Outline each Plasmodium falciparum-infected red blood cell.
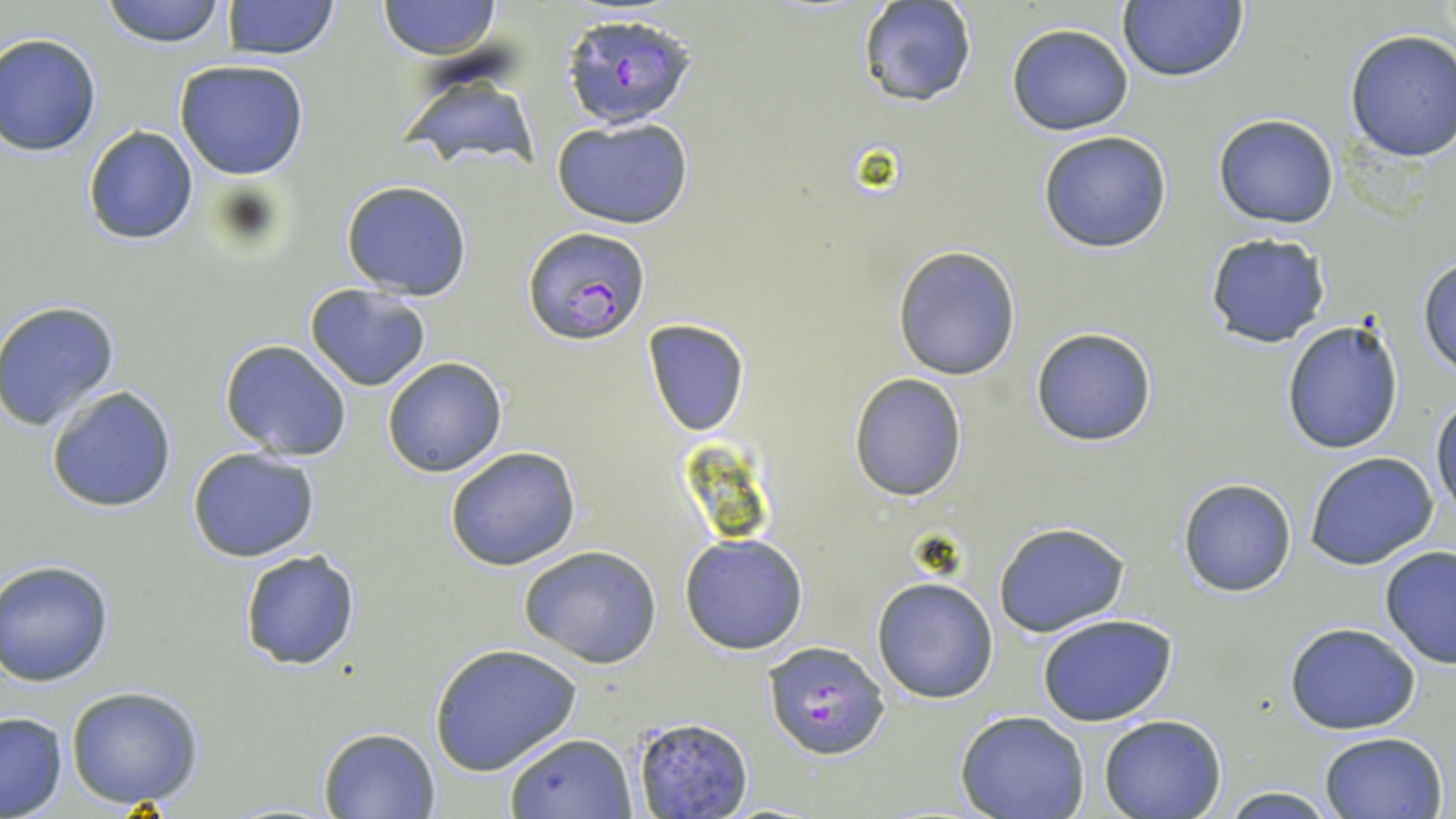
Approximate bounding boxes as (x1, y1, x2, y2) in pixels.
Plasmodium falciparum-infected red blood cells: (561, 12, 698, 132), (521, 227, 649, 346), (762, 641, 892, 760).

Uninfected red blood cell locations: (99, 0, 229, 48), (225, 0, 339, 60), (378, 0, 502, 58), (856, 0, 975, 108), (1116, 2, 1249, 84), (1006, 24, 1134, 135), (1343, 28, 1456, 162), (0, 33, 102, 157), (174, 59, 309, 180), (399, 64, 544, 176), (1212, 113, 1340, 229), (552, 116, 694, 229), (82, 125, 198, 245), (1036, 130, 1172, 253), (340, 180, 474, 300), (1203, 232, 1332, 349), (892, 245, 1022, 380), (1418, 253, 1456, 378), (304, 284, 432, 392), (0, 302, 121, 432), (1280, 317, 1404, 455), (642, 319, 750, 436), (1029, 326, 1159, 447), (219, 339, 353, 460), (382, 356, 509, 477), (847, 372, 967, 502), (45, 384, 179, 514), (1430, 393, 1455, 520), (187, 446, 322, 563), (444, 446, 582, 571), (1304, 451, 1439, 569), (1177, 478, 1297, 598), (992, 521, 1130, 638), (680, 534, 808, 654), (520, 545, 662, 667), (1378, 545, 1456, 668), (237, 548, 363, 670), (0, 561, 114, 686), (872, 575, 999, 704), (1038, 614, 1177, 727), (1284, 622, 1422, 734), (429, 641, 583, 777), (63, 686, 206, 808), (0, 710, 68, 818), (957, 712, 1091, 819), (1098, 715, 1226, 819), (631, 716, 754, 819), (318, 727, 440, 817), (1317, 730, 1449, 819), (503, 733, 637, 818), (1214, 785, 1340, 819). Slide-level diagnosis: Plasmodium falciparum. Thin blood smear. May-Grünwald-Giemsa-stained preparation. Captured at 1000x magnification. Image is 1456×819 pixels. Light microscopy. Single field of view.